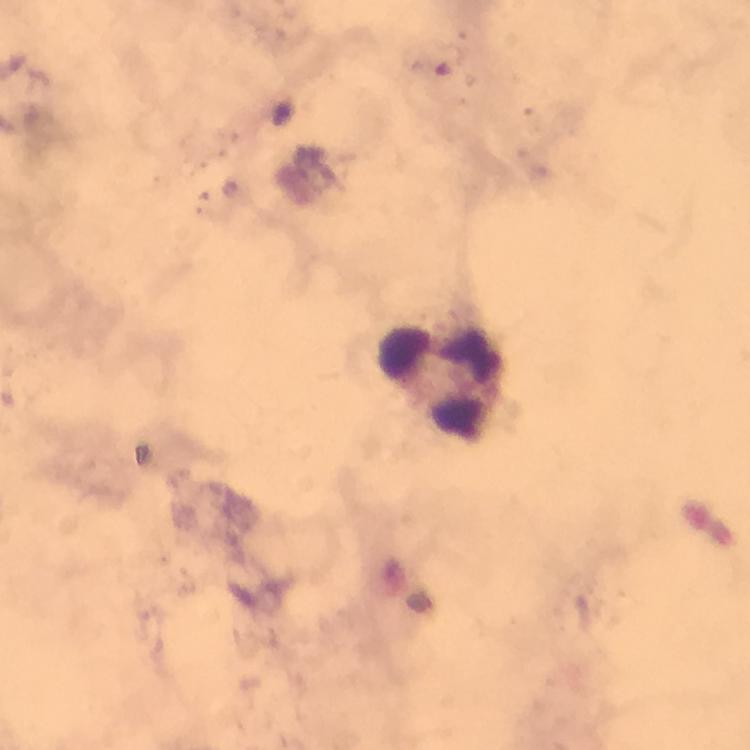
Approximate object centers, in pixels from the top-left corner.
Summary:
  - Leukocyte locations: (x=440, y=378)
  - Immersion oil: used
  - Magnification: 100x
  - Context: from a malaria diagnostic workup
  - Stain: Giemsa
  - Image size: 750×750 pixels
  - Capture: smartphone camera through the microscope
  - Preparation: thick smear
  - Cropped from: one field of view
  - Plasmodium parasites: none seen